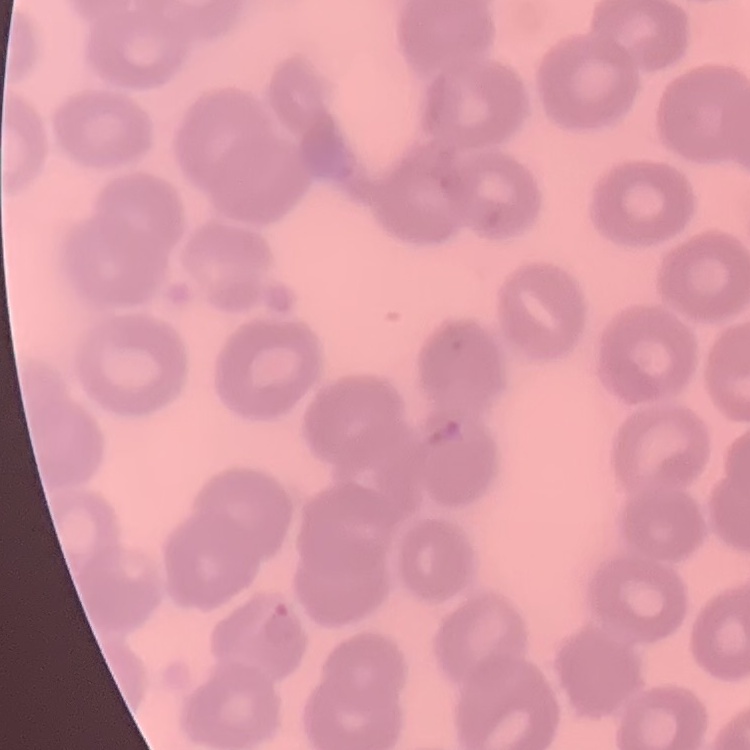

Summary:
  - Red blood cell morphology: no rouleaux formation
  - Preparation: thin blood smear
  - Image type: one tile cut from a larger photomicrograph
  - Stain: Field's or Giemsa